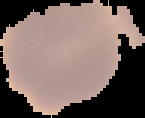
The area outside the segmented cell region is set to black. Malaria status: uninfected. From a thin blood smear. Image is 145×118 pixels.